Report the malaria status of this cell.
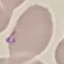
It is uninfected.

stain = Giemsa
capture = smartphone camera at the microscope eyepiece
image type = cell patch, automatically extracted from a larger field of view and resized to 64 × 64 pixels
preparation = thin smear